Classify this cell by malaria status.
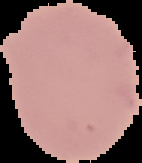

It is uninfected.

Summary:
  - Image type: cell region segmented out of the field of view; surrounding area masked to black
  - Image size: 142×163 pixels
  - Preparation: thin blood smear